State the blood parasite species.
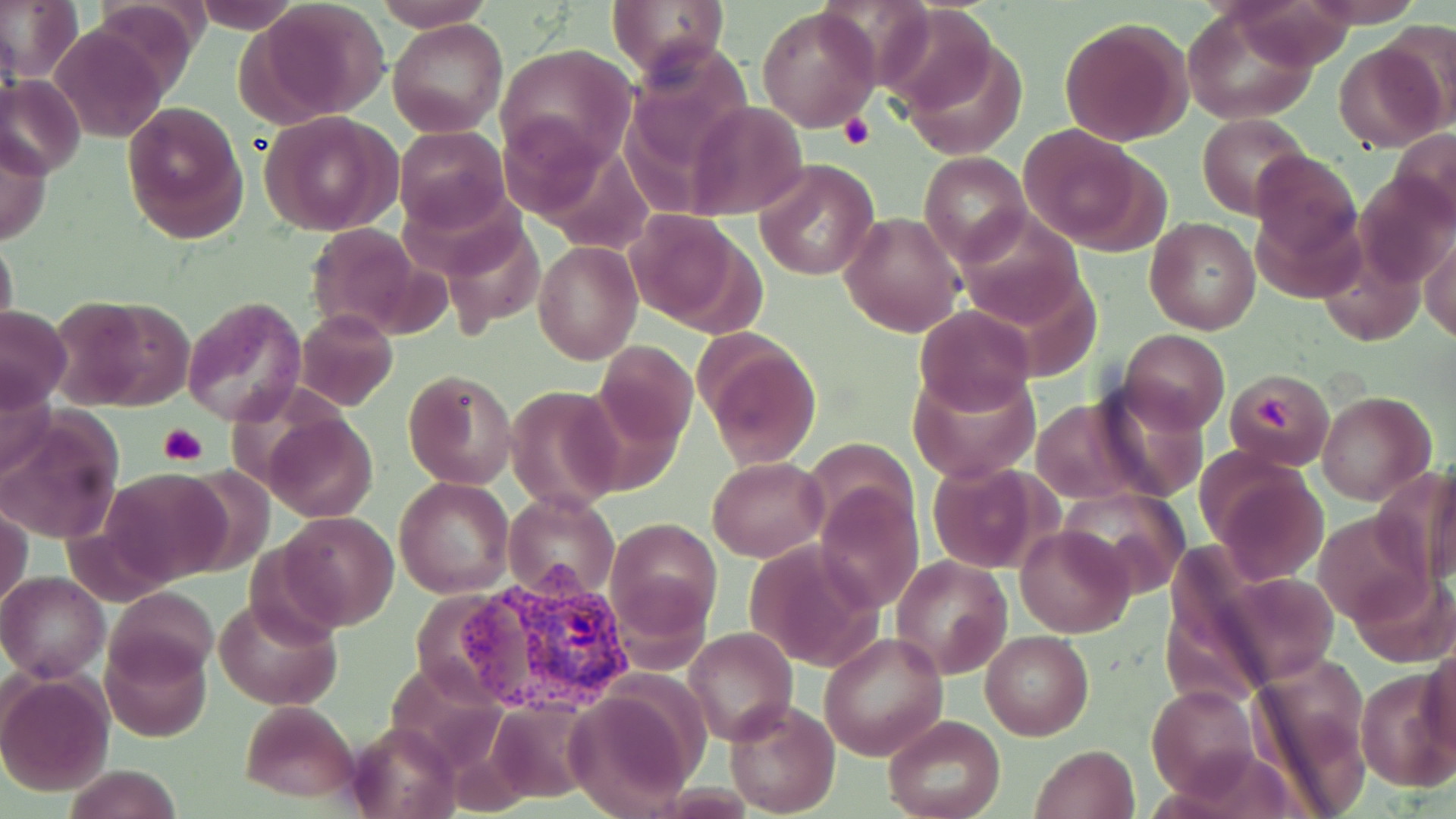

Plasmodium vivax.

Summary:
  - Coordinate format: approximate bounding boxes as (x1,y1)-(x2,y2) corner pairs in pixels
  - Plasmodium vivax-infected red blood cell locations: (453,558)-(637,716)
  - Platelet locations: (839,113)-(875,151), (1253,395)-(1298,436), (159,422)-(207,466)
  - Uninfected red blood cell locations: (2,0)-(83,87), (373,0)-(496,30), (607,0)-(728,77), (1296,0)-(1429,26), (186,1)-(306,32), (255,1)-(390,119), (757,5)-(880,131), (1181,8)-(1321,125), (881,10)-(1013,142), (1058,16)-(1192,147), (388,19)-(507,136), (1381,23)-(1456,130), (51,24)-(169,144), (1333,40)-(1447,152), (495,42)-(638,169), (1,75)-(83,176), (123,101)-(250,244), (686,101)-(810,220), (259,111)-(402,236), (1198,113)-(1311,220), (1016,122)-(1155,251), (393,125)-(510,233), (1390,128)-(1456,227), (0,132)-(51,247), (1250,148)-(1363,277), (918,153)-(1030,264), (754,159)-(877,282), (955,208)-(1088,331), (624,210)-(754,332), (839,212)-(966,337), (442,218)-(545,332), (1145,218)-(1261,335), (306,223)-(434,341), (1,231)-(18,342), (1422,233)-(1455,345), (533,241)-(643,365), (55,291)-(195,410), (181,298)-(309,427), (0,304)-(72,410), (914,305)-(1037,415), (294,308)-(397,411), (1119,329)-(1229,433), (696,335)-(823,469), (594,340)-(696,454), (909,366)-(1039,482), (1224,368)-(1333,470), (402,369)-(518,490), (1086,379)-(1212,504), (0,380)-(54,488), (505,385)-(625,513), (1318,391)-(1436,505), (1025,396)-(1161,505), (2,411)-(124,547), (263,414)-(378,523), (807,438)-(915,536), (1200,454)-(1330,583), (708,456)-(827,562), (1409,463)-(1456,589), (925,464)-(1048,573), (101,468)-(231,585), (394,477)-(515,598), (812,484)-(923,612), (1056,486)-(1191,599), (506,491)-(618,602), (1,506)-(31,614), (1314,509)-(1434,628), (274,511)-(399,630), (607,517)-(722,635), (1016,525)-(1136,638), (744,540)-(882,673), (890,555)-(1011,678), (1350,565)-(1455,668), (0,571)-(109,681), (105,584)-(219,688), (216,594)-(342,710), (684,628)-(796,745), (981,629)-(1093,741), (819,630)-(948,761), (101,635)-(211,742), (1421,646)-(1455,758), (1246,655)-(1373,810), (383,661)-(509,767), (1356,667)-(1456,791), (1,672)-(114,795), (1148,684)-(1262,799), (566,689)-(699,817), (238,699)-(363,802), (724,699)-(841,817), (487,700)-(596,803), (881,715)-(1005,819), (348,720)-(459,819), (1031,744)-(1140,819), (63,764)-(183,819)
  - Preparation: thin blood film
  - Stain: May-Grünwald-Giemsa
  - Image size: 1456×819 pixels
  - Modality: optical microscopy
  - Magnification: 1000x
  - Field of view: one of a larger specimen